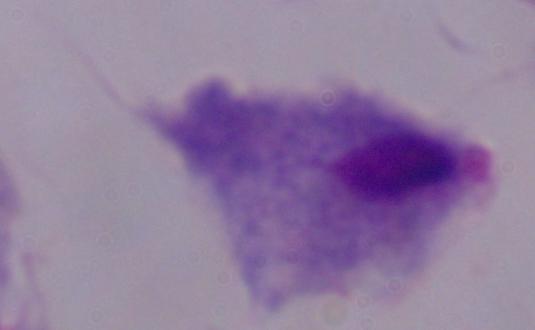

modality = micrograph
magnification = 1000x
identification = trichomonad